Report the malaria status of this cell.
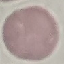

It is uninfected.

Summary:
  - Stain: Giemsa
  - Capture: smartphone through the microscope eyepiece
  - Image type: cell patch, automatically extracted from a larger field of view and resized to 64 × 64 pixels
  - Preparation: thin smear